Identify the parasite.
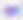

This is Toxoplasma gondii.

magnification = 400x
modality = micrograph